Name the cell type shown.
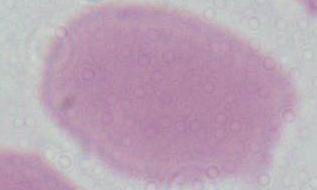
This is an erythrocyte.

Summary:
  - Magnification: 1000x
  - Modality: micrograph